Report the malaria status of this cell.
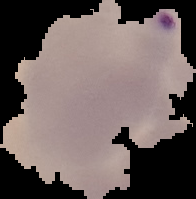
Parasitized.

Summary:
  - Image type: cell region segmented out of the field of view; surrounding area masked to black
  - Image size: 196×199 pixels
  - Preparation: thin blood smear